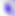
Toxoplasma gondii is seen. 400x magnification. Photomicrograph.